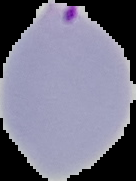 Cell region segmented out of the field of view; the surrounding area is masked to black. From a thin blood film. Image is 136×181 pixels. Result: Plasmodium parasites identified.